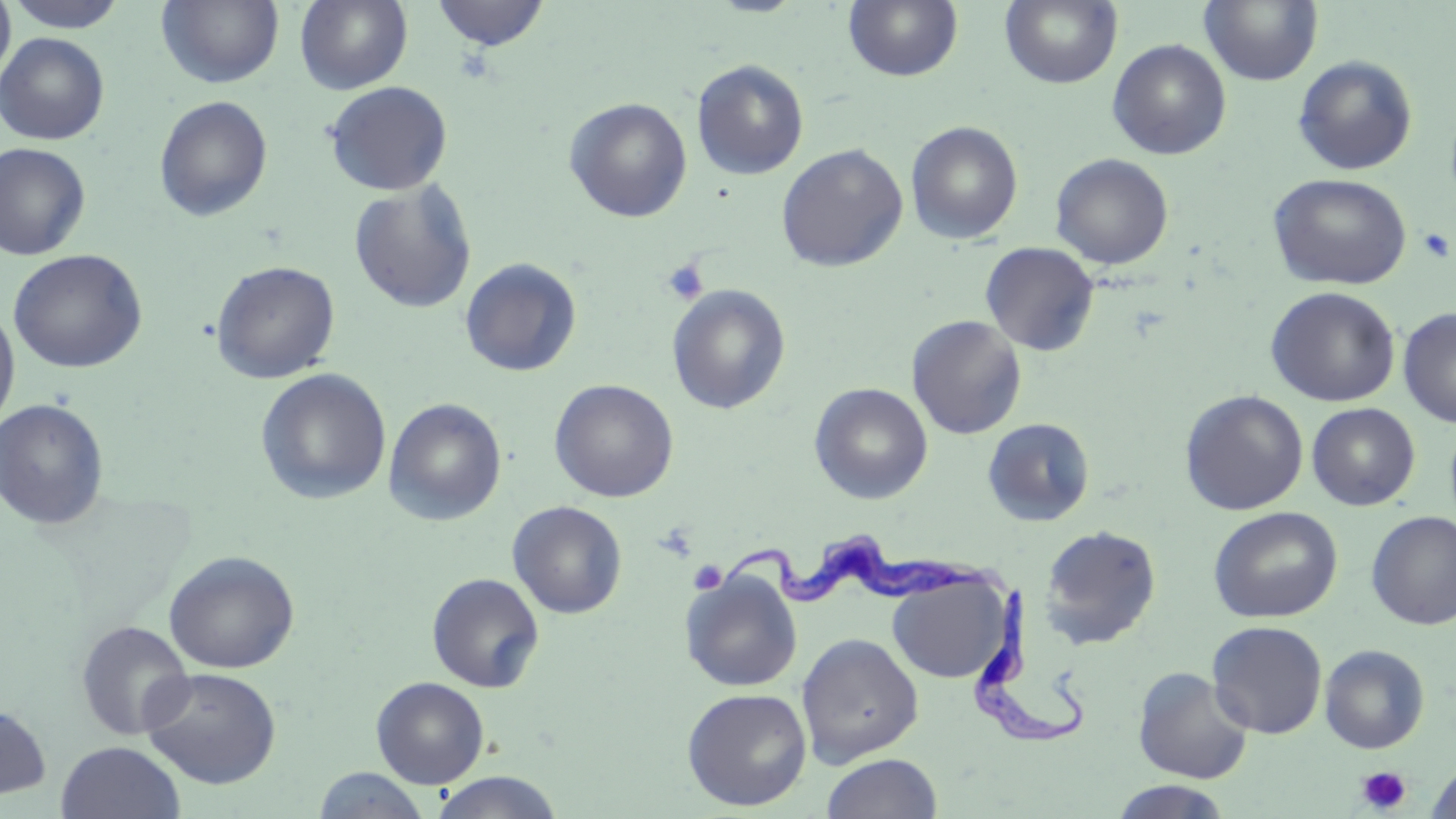

Summary:
  - Coordinate format: approximate bounding boxes as (x1,y1)-(x2,y2) corner pairs in pixels
  - Platelet locations: (1416,227)-(1455,263), (661,259)-(708,305), (688,560)-(727,595), (1356,766)-(1411,814)
  - Trypanosoma brucei locations: (709,531)-(1011,610), (972,583)-(1094,753)
  - Uninfected red blood cell locations: (0,0)-(16,86), (3,0)-(131,33), (157,0)-(284,88), (294,0)-(413,94), (429,1)-(551,52), (844,1)-(963,83), (1000,1)-(1122,88), (1200,1)-(1323,86), (0,32)-(109,145), (1107,39)-(1231,160), (1293,55)-(1418,176), (692,59)-(809,180), (323,81)-(454,196), (154,96)-(273,222), (564,97)-(693,223), (906,120)-(1023,244), (0,142)-(91,260), (776,143)-(908,272), (1051,153)-(1173,270), (1268,173)-(1413,289), (349,180)-(478,314), (980,241)-(1100,356), (9,249)-(148,373), (460,258)-(582,378), (210,261)-(340,384), (666,284)-(791,414), (1265,286)-(1400,407), (0,303)-(20,434), (1398,307)-(1456,428), (907,315)-(1027,439), (255,368)-(391,505), (549,379)-(679,502), (809,382)-(932,504), (1180,390)-(1308,515), (0,398)-(109,530), (384,398)-(507,525), (1306,403)-(1420,510), (983,418)-(1095,526), (507,501)-(627,619), (1208,506)-(1343,624), (1366,510)-(1456,630), (1039,524)-(1162,650), (163,550)-(299,673), (680,570)-(803,693), (426,572)-(545,693), (887,572)-(1010,684), (76,620)-(194,740), (1207,621)-(1328,739), (796,632)-(923,767), (1319,644)-(1429,754), (140,667)-(282,790), (1133,667)-(1254,784), (371,676)-(489,787), (681,687)-(812,811), (0,702)-(52,800), (56,740)-(186,819), (820,752)-(942,819), (1425,763)-(1456,819), (311,767)-(432,818), (428,771)-(565,818), (1109,781)-(1234,819)
  - Slide-level diagnosis: Trypanosoma brucei
  - Preparation: thin blood film
  - Modality: optical microscopy
  - Field of view: single
  - Magnification: 1000x
  - Image size: 1456×819 pixels
  - Stain: May-Grünwald-Giemsa